Comment on the morphology of the erythrocytes.
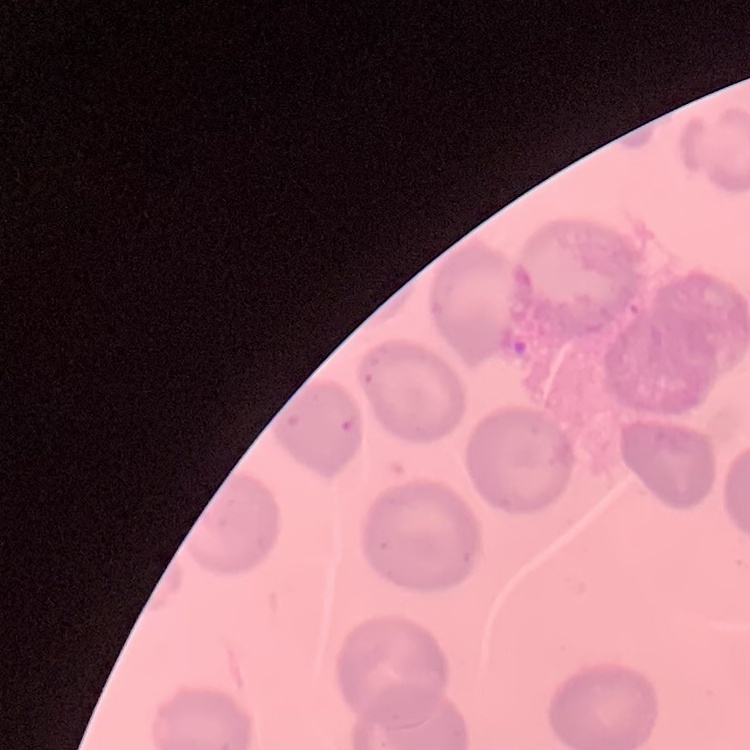

They show no rouleaux formation.

Thin blood smear. Square crop of a larger photomicrograph. Field's or Giemsa stain.